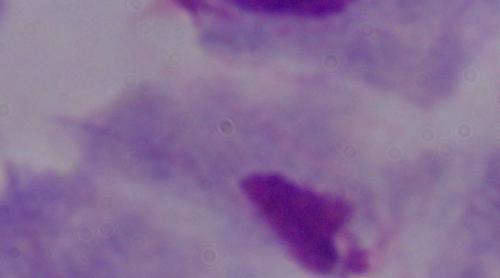
A trichomonad is shown. Captured at 1000x magnification. Micrograph.